Name the parasite shown.
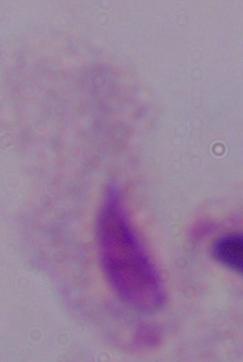

A trichomonad.

Micrograph. Captured at 1000x magnification.